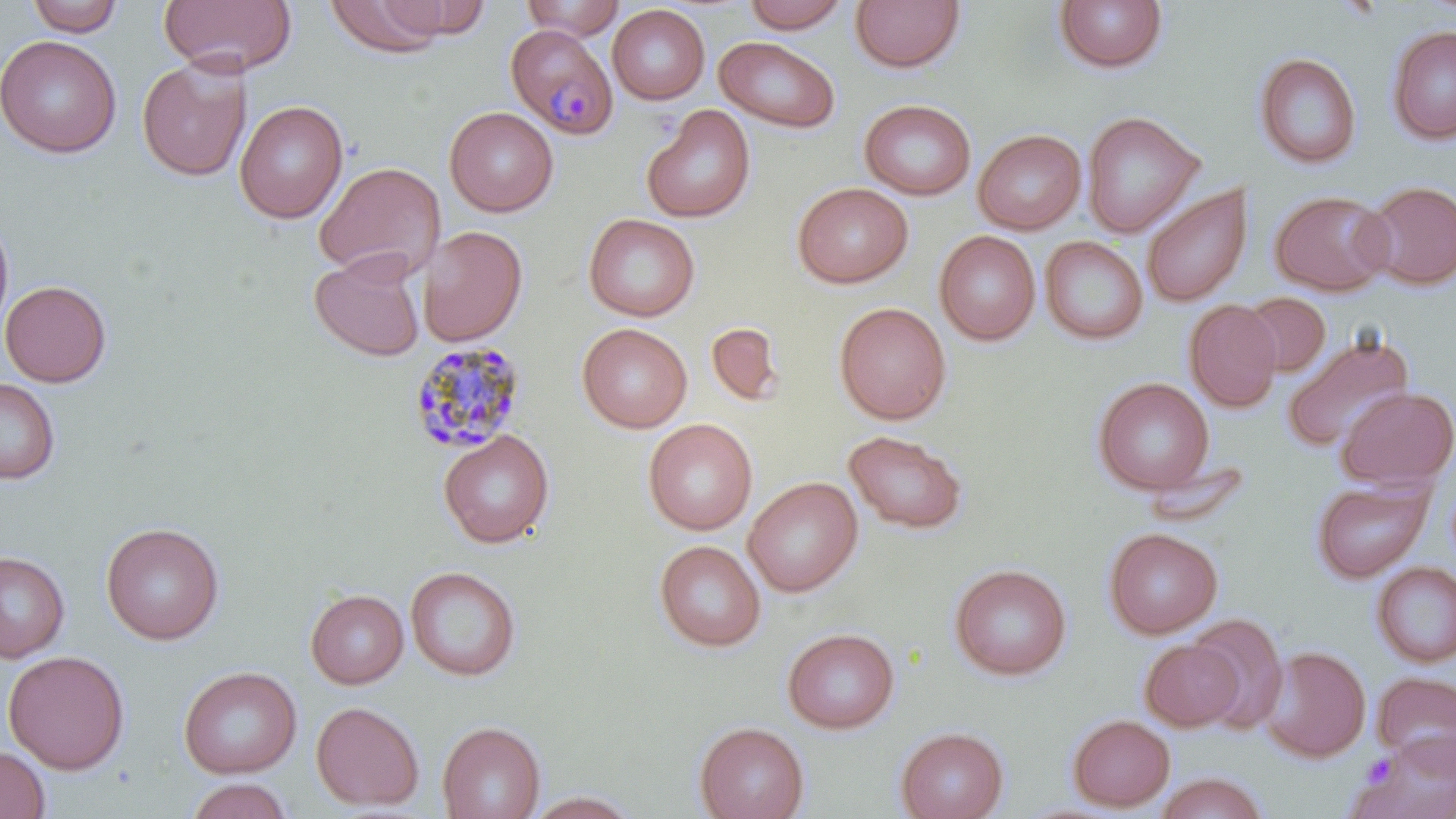

{
  "slide_level_diagnosis": "Plasmodium malariae",
  "preparation": "thin blood smear",
  "field_of_view": "single",
  "platelet_locations": "approximate bounding boxes as [x1, y1, x2, y2] in pixels: [1363, 755, 1397, 789]",
  "magnification": "1000x",
  "stain": "May-Grünwald-Giemsa",
  "plasmodium_malariae_infected_red_blood_cell_locations": "approximate bounding boxes as [x1, y1, x2, y2] in pixels: [505, 23, 618, 139], [408, 340, 526, 454]",
  "image_size": "1456×819 pixels",
  "uninfected_red_blood_cell_locations": "approximate bounding boxes as [x1, y1, x2, y2] in pixels: [25, 0, 124, 36], [159, 0, 297, 77], [324, 0, 449, 57], [520, 0, 626, 41], [378, 1, 491, 39], [743, 1, 851, 34], [850, 1, 966, 74], [1054, 1, 1168, 75], [608, 4, 710, 105], [1386, 24, 1456, 145], [1, 34, 121, 158], [714, 36, 841, 134], [1254, 52, 1362, 170], [136, 56, 252, 182], [859, 98, 977, 200], [234, 100, 348, 224], [445, 106, 559, 216], [642, 106, 756, 223], [1082, 111, 1204, 238], [973, 129, 1087, 234], [314, 161, 446, 283], [1362, 180, 1456, 290], [792, 181, 913, 289], [1141, 185, 1253, 307], [1269, 190, 1394, 295], [583, 213, 700, 322], [0, 214, 15, 340], [418, 226, 527, 346], [934, 230, 1041, 345], [1040, 236, 1148, 345], [310, 250, 426, 362], [0, 280, 111, 387], [1242, 292, 1330, 375], [1184, 300, 1282, 412], [834, 301, 951, 425], [706, 322, 785, 406], [577, 323, 692, 433], [1282, 332, 1415, 455], [0, 377, 60, 484], [1093, 377, 1214, 496], [1336, 386, 1455, 490], [643, 418, 758, 536], [438, 430, 555, 548], [843, 430, 967, 535], [743, 476, 863, 597], [1310, 476, 1434, 583], [101, 521, 225, 645], [1103, 527, 1222, 639], [654, 540, 766, 652], [0, 548, 88, 759], [0, 551, 70, 662], [1371, 560, 1456, 668], [950, 563, 1072, 681], [405, 566, 521, 681], [306, 589, 408, 688], [1187, 613, 1288, 733], [782, 626, 900, 733], [1140, 639, 1244, 731], [1259, 646, 1371, 763], [3, 650, 129, 774], [178, 665, 302, 778], [1372, 670, 1456, 771], [311, 700, 425, 811], [1067, 713, 1175, 811], [437, 720, 546, 819], [694, 721, 809, 819], [895, 726, 1009, 819], [1351, 733, 1456, 819], [0, 744, 51, 818], [1152, 772, 1270, 818], [184, 777, 294, 819], [525, 791, 642, 818]",
  "modality": "optical microscopy"
}